Report the malaria status.
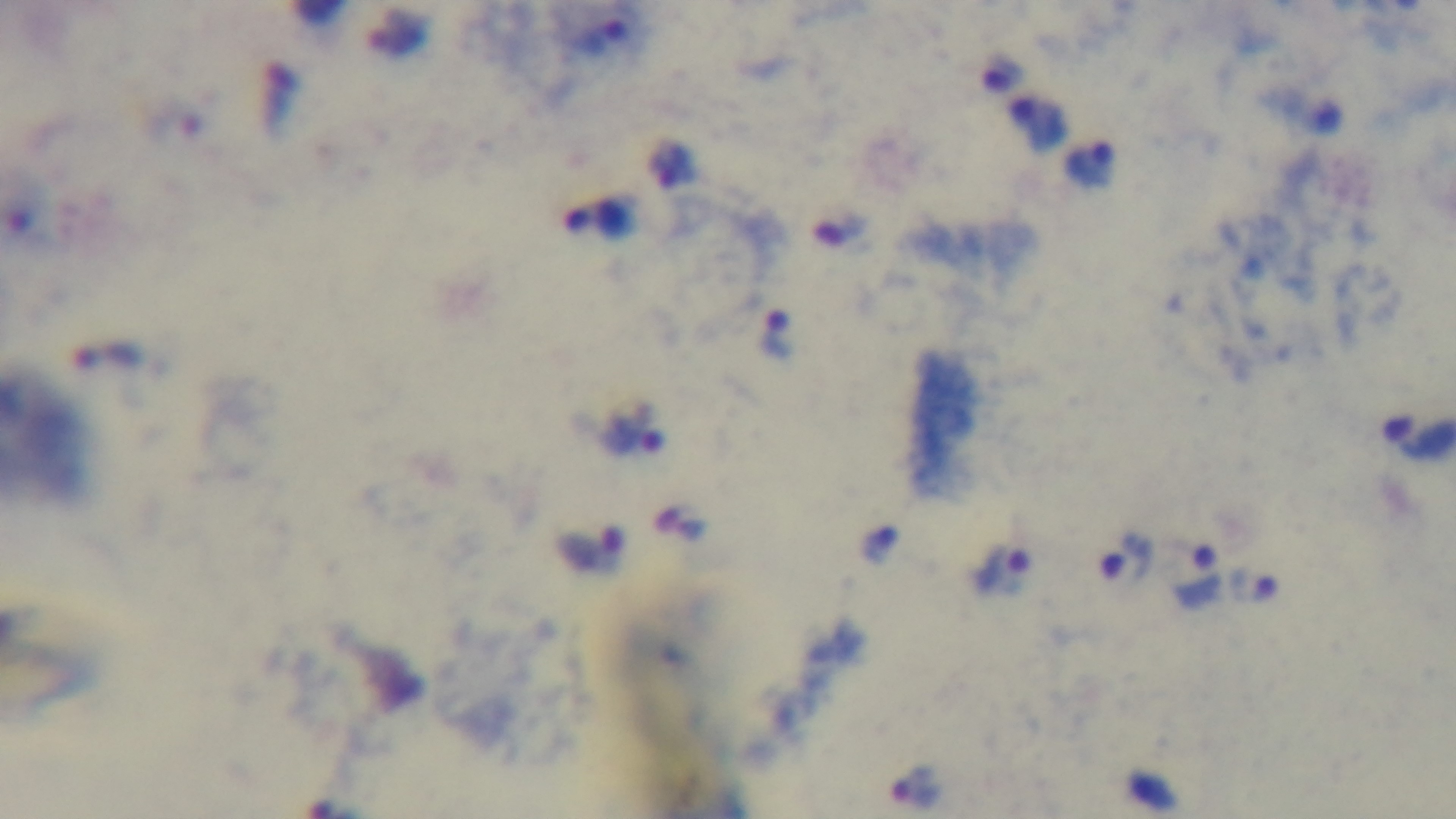

Infected.

capture: mounted 4K digital camera
objective: 100x oil immersion
stain: Giemsa
field_of_view: single
modality: light microscopy
preparation: thick